Classify this cell by malaria status.
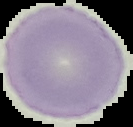

Uninfected.

image_size: 133×127 pixels
image_type: segmented cell region with the area outside set to black
preparation: thin blood film